Point out each Plasmodium parasite.
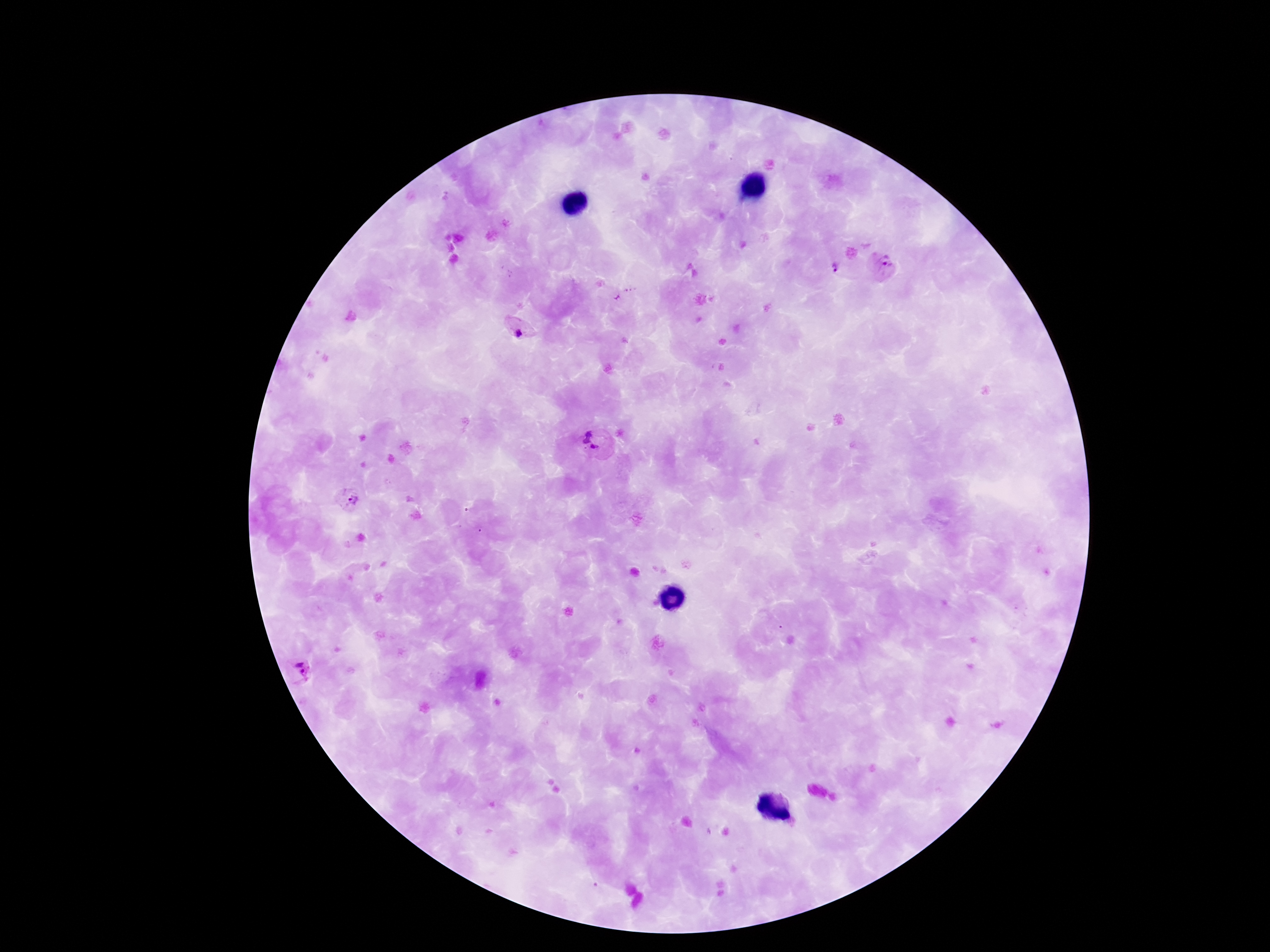

Approximate centers as [x, y] in pixels.
Plasmodium parasites: [883, 265], [832, 268], [519, 329], [594, 442], [349, 500], [297, 670].

Giemsa-stained preparation. Photographed through the microscope eyepiece with a smartphone camera. Image is 1270×952 pixels. 100x magnification. Thick blood smear. Patient malaria status: infected. Single field of view.